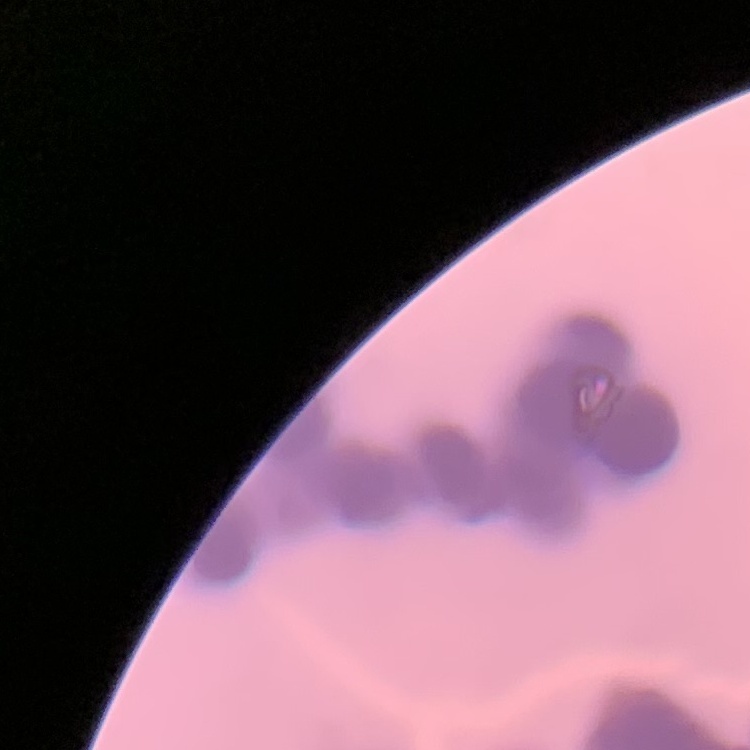
red blood cell morphology = rouleaux formation
image type = one tile cut from a larger photomicrograph
preparation = thin blood film
stain = Field's or Giemsa